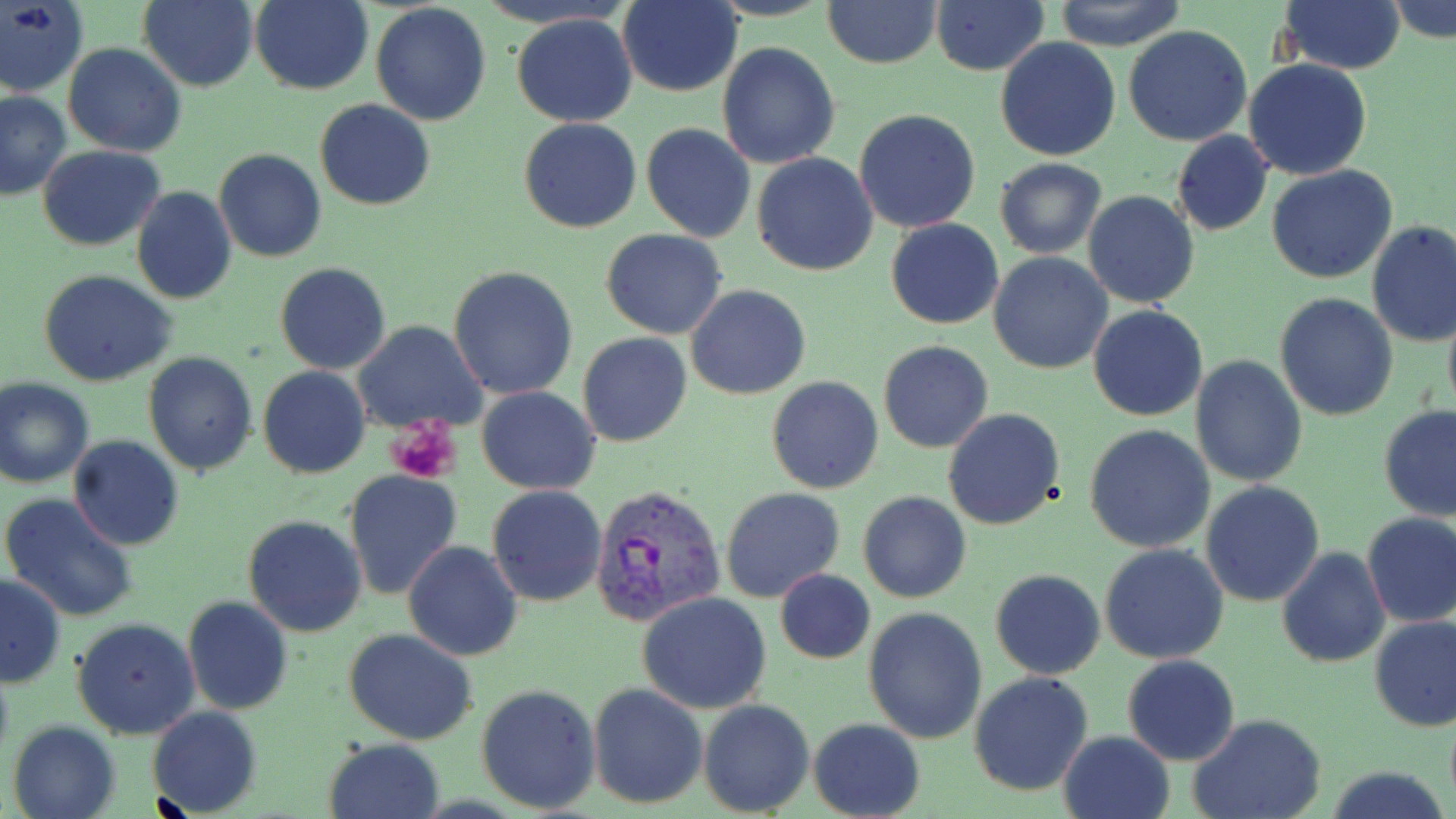

Summary:
  - Coordinate format: approximate bounding boxes as [x1, y1, x2, y2] in pixels
  - Plasmodium vivax-infected red blood cell locations: [590, 483, 723, 624]
  - Platelet locations: [387, 419, 463, 485]
  - Uninfected red blood cell locations: [0, 0, 89, 98], [137, 0, 259, 91], [248, 0, 373, 94], [822, 0, 941, 69], [1052, 0, 1186, 51], [1277, 0, 1405, 74], [1386, 0, 1456, 44], [617, 1, 743, 97], [931, 1, 1049, 75], [370, 4, 491, 126], [510, 12, 639, 127], [1122, 25, 1252, 147], [995, 37, 1122, 161], [717, 41, 840, 170], [64, 43, 186, 158], [1243, 59, 1373, 181], [0, 89, 71, 198], [315, 100, 435, 211], [854, 108, 982, 233], [519, 118, 642, 234], [641, 123, 756, 243], [1171, 130, 1275, 236], [37, 146, 165, 251], [213, 149, 327, 262], [752, 151, 878, 277], [994, 157, 1107, 258], [1267, 165, 1396, 284], [131, 186, 238, 304], [1082, 191, 1200, 309], [886, 219, 1003, 330], [1367, 221, 1456, 350], [602, 230, 729, 340], [989, 252, 1113, 374], [276, 262, 390, 374], [448, 265, 580, 399], [39, 271, 178, 388], [686, 284, 812, 400], [1275, 294, 1400, 422], [1442, 301, 1456, 421], [1088, 304, 1209, 422], [354, 321, 487, 433], [578, 332, 692, 448], [878, 340, 994, 453], [143, 352, 259, 474], [1190, 356, 1308, 487], [258, 366, 370, 478], [766, 375, 885, 494], [2, 378, 96, 490], [477, 386, 600, 494], [1378, 404, 1456, 522], [944, 408, 1067, 530], [1085, 423, 1216, 554], [67, 436, 184, 551], [343, 470, 463, 599], [1200, 480, 1325, 606], [487, 484, 607, 607], [721, 487, 846, 604], [858, 491, 971, 604], [2, 493, 140, 621], [1361, 511, 1456, 629], [242, 514, 368, 637], [402, 541, 523, 662], [1099, 544, 1230, 664], [1278, 547, 1390, 666], [990, 568, 1106, 680], [774, 569, 875, 663], [0, 574, 67, 689], [638, 592, 771, 714], [182, 596, 294, 715], [862, 606, 987, 744], [1369, 615, 1456, 732], [72, 617, 200, 738], [344, 629, 478, 747], [1123, 654, 1240, 765], [968, 671, 1094, 795], [476, 683, 601, 814], [588, 683, 707, 809], [699, 699, 815, 817], [148, 706, 261, 817], [1190, 714, 1326, 819], [808, 718, 926, 819], [7, 720, 120, 819], [1059, 731, 1174, 819], [324, 738, 445, 819], [1325, 766, 1451, 819]
  - Slide-level diagnosis: Plasmodium vivax
  - Preparation: thin blood film
  - Stain: May-Grünwald-Giemsa
  - Field of view: one of a larger specimen
  - Magnification: 1000x
  - Modality: optical microscopy
  - Image size: 1456×819 pixels